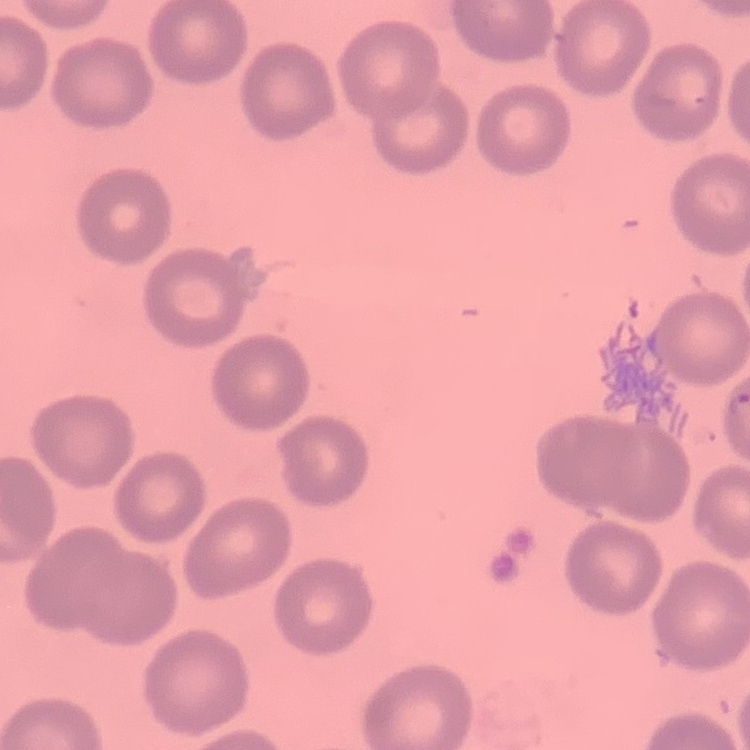

{
  "red_blood_cell_morphology": "no rouleaux formation",
  "image_type": "one tile cut from a larger photomicrograph",
  "stain": "Field's or Giemsa",
  "preparation": "thin peripheral smear"
}